Locate every blood parasite and identify its species.
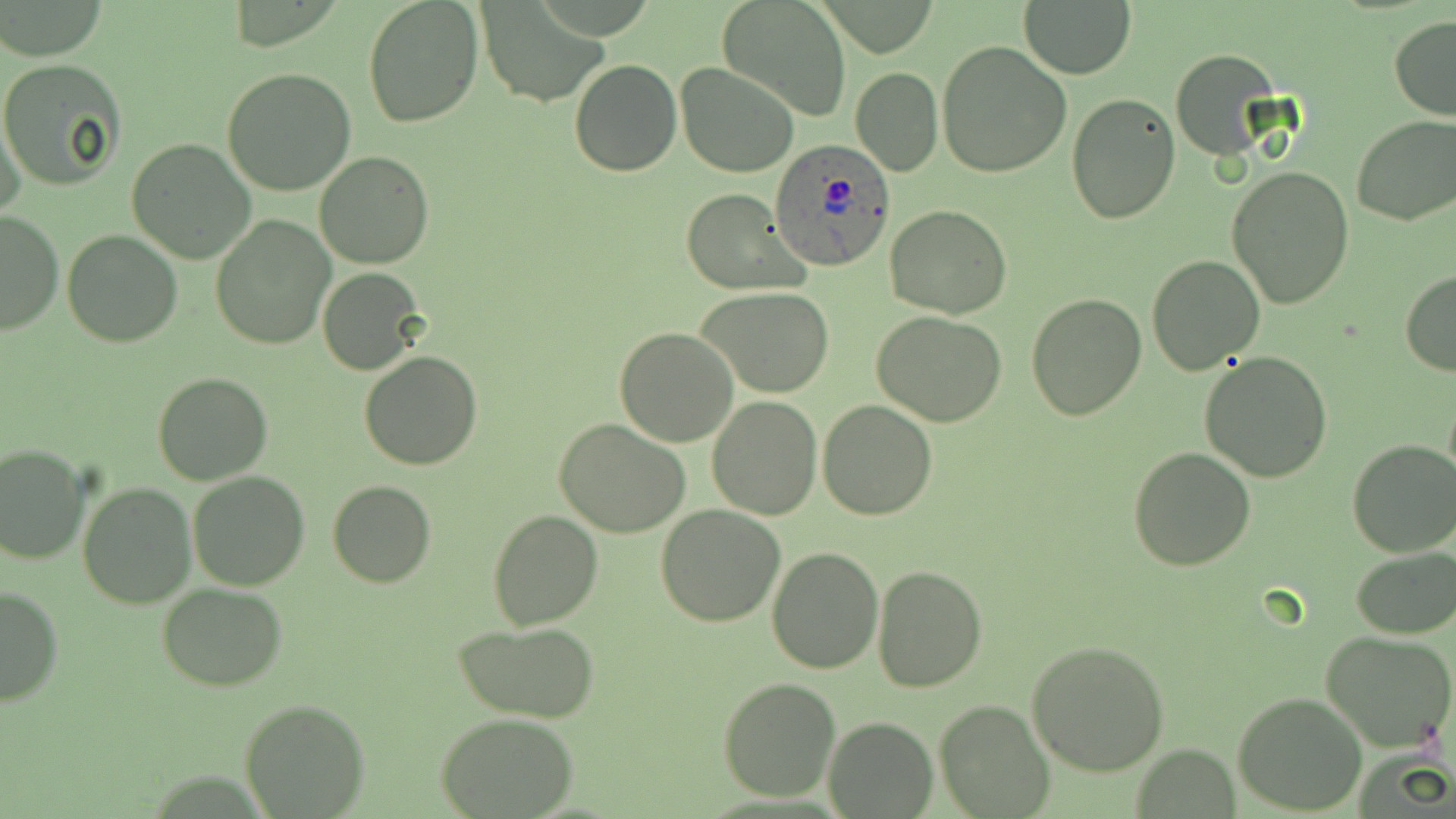
Approximate bounding boxes as [x1, y1, x2, y2] in pixels.
Plasmodium ovale-infected red blood cells: [769, 140, 895, 272].
No Plasmodium falciparum, Plasmodium malariae, Plasmodium vivax, Babesia divergens, or Trypanosoma brucei observed.

slide-level diagnosis = Plasmodium ovale
image size = 1456×819 pixels
preparation = thin blood film
stain = May-Grünwald-Giemsa
magnification = 1000x
field of view = single
uninfected red blood cell locations = approximate bounding boxes as [x1, y1, x2, y2] in pixels: [362, 0, 484, 127], [716, 0, 852, 121], [1019, 0, 1138, 79], [480, 5, 608, 107], [1388, 16, 1456, 121], [938, 39, 1072, 176], [1171, 49, 1280, 160], [0, 58, 129, 190], [569, 58, 681, 176], [677, 63, 800, 179], [221, 68, 356, 195], [851, 68, 943, 176], [1065, 93, 1180, 226], [1, 110, 27, 219], [1351, 115, 1456, 227], [126, 138, 255, 263], [314, 151, 434, 269], [1226, 165, 1354, 307], [684, 190, 808, 296], [885, 204, 1012, 319], [0, 210, 62, 335], [210, 218, 334, 350], [63, 228, 181, 347], [1145, 254, 1266, 374], [317, 268, 425, 375], [1400, 270, 1456, 376], [695, 286, 836, 399], [1026, 294, 1146, 422], [871, 310, 1007, 426], [614, 327, 740, 447], [359, 351, 483, 470], [1199, 351, 1333, 482], [151, 372, 273, 486], [708, 395, 822, 520], [817, 399, 939, 520], [555, 418, 694, 538], [1346, 439, 1456, 558], [0, 443, 88, 565], [1128, 446, 1257, 571], [188, 472, 310, 588], [327, 480, 437, 587], [78, 482, 197, 608], [656, 505, 785, 625], [486, 509, 604, 630], [766, 546, 883, 674], [1351, 548, 1456, 638], [872, 564, 987, 693], [157, 583, 288, 691], [0, 585, 65, 708], [454, 622, 598, 723], [1320, 629, 1456, 751], [1026, 638, 1171, 776], [718, 678, 840, 802], [1232, 689, 1367, 814], [239, 699, 370, 818], [934, 700, 1055, 819], [436, 713, 579, 818], [824, 716, 937, 817]
modality = optical microscopy